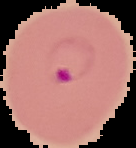
Summary:
  - Image type: segmented cell region with the area outside set to black
  - Image size: 136×148 pixels
  - Malaria status: parasitized
  - Preparation: thin blood smear